Identify the blood parasite species.
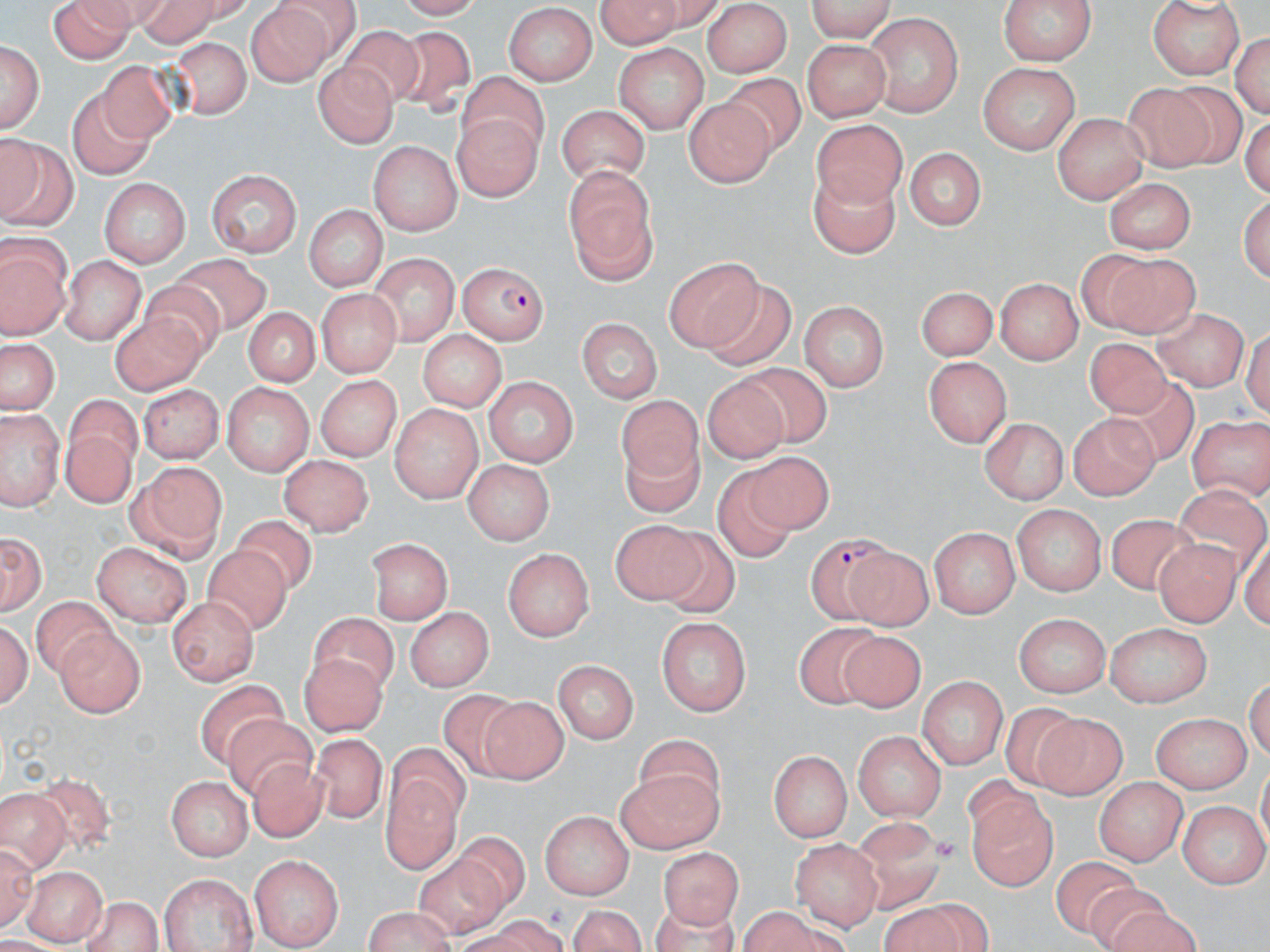

Plasmodium falciparum.

{
  "preparation": "thin blood film",
  "modality": "light microscopy",
  "stain": "May-Grünwald-Giemsa",
  "magnification": "1000x",
  "field_of_view": "one of a larger specimen",
  "image_size": "1270×952 pixels",
  "uninfected_red_blood_cell_locations": "approximate bounding boxes as [x1, y1, x2, y2] in pixels: [47, 0, 133, 63], [126, 0, 220, 46], [592, 0, 722, 41], [800, 0, 896, 40], [1150, 0, 1246, 80], [994, 1, 1101, 64], [250, 2, 343, 83], [505, 5, 595, 84], [705, 7, 789, 74], [865, 14, 967, 117], [339, 21, 424, 113], [396, 26, 477, 119], [1233, 30, 1267, 120], [1, 37, 46, 138], [800, 37, 894, 118], [171, 38, 253, 120], [614, 41, 708, 134], [95, 59, 172, 143], [312, 61, 395, 148], [981, 63, 1078, 153], [457, 70, 545, 166], [724, 73, 813, 158], [1160, 83, 1248, 163], [1123, 87, 1216, 171], [71, 90, 156, 177], [685, 95, 773, 189], [556, 101, 656, 189], [453, 108, 543, 204], [1052, 113, 1150, 199], [811, 120, 908, 206], [0, 133, 69, 233], [368, 138, 462, 236], [907, 143, 987, 230], [562, 162, 663, 286], [810, 165, 901, 268], [207, 169, 302, 258], [1103, 175, 1196, 253], [103, 179, 190, 266], [305, 204, 385, 292], [1, 234, 72, 339], [1085, 248, 1198, 334], [665, 254, 764, 349], [172, 255, 271, 323], [368, 255, 458, 349], [59, 256, 144, 343], [699, 275, 793, 368], [992, 277, 1085, 363], [137, 281, 225, 356], [915, 284, 998, 359], [315, 288, 405, 375], [798, 301, 889, 392], [242, 307, 324, 388], [1154, 309, 1246, 391], [111, 313, 208, 400], [580, 318, 661, 403], [418, 331, 505, 413], [2, 338, 55, 415], [1080, 339, 1175, 421], [923, 354, 1015, 447], [742, 363, 839, 445], [701, 374, 790, 463], [314, 376, 397, 461], [1101, 376, 1199, 469], [483, 377, 580, 470], [139, 384, 221, 462], [222, 385, 312, 474], [331, 386, 459, 474], [615, 390, 708, 481], [60, 398, 142, 510], [391, 403, 482, 502], [2, 410, 60, 508], [1069, 414, 1157, 500], [977, 417, 1071, 502], [1186, 418, 1270, 503], [621, 431, 702, 517], [741, 452, 835, 535], [277, 455, 371, 537], [463, 459, 554, 546], [137, 464, 226, 544], [714, 465, 800, 562], [1176, 484, 1268, 576], [1013, 503, 1103, 598], [231, 511, 324, 585], [1106, 515, 1201, 596], [609, 520, 709, 609], [928, 524, 1021, 616], [655, 526, 743, 615], [1, 529, 46, 616], [366, 535, 454, 621], [1153, 540, 1246, 626], [868, 541, 931, 630], [93, 542, 192, 625], [201, 543, 294, 636], [502, 547, 592, 643], [167, 593, 257, 687], [30, 594, 115, 680], [402, 606, 496, 689], [306, 610, 403, 694], [1015, 612, 1111, 699], [1, 613, 35, 713], [656, 616, 751, 714], [791, 619, 885, 719], [1107, 621, 1213, 707], [53, 626, 145, 716], [836, 631, 927, 715], [298, 656, 392, 735], [551, 657, 639, 742], [918, 674, 1005, 772], [196, 682, 288, 764], [433, 690, 528, 778], [483, 692, 565, 785], [1003, 703, 1090, 791], [220, 711, 319, 801], [1153, 712, 1253, 792], [1034, 716, 1126, 800], [854, 729, 944, 823], [634, 735, 726, 823], [313, 736, 389, 825], [771, 747, 852, 841], [246, 755, 335, 842], [615, 764, 721, 852], [387, 767, 461, 873], [40, 772, 119, 854], [168, 773, 253, 858], [1096, 773, 1188, 865], [0, 787, 72, 878], [967, 798, 1057, 893], [1180, 803, 1268, 886], [540, 810, 633, 900], [847, 817, 946, 915], [456, 828, 533, 911], [793, 842, 881, 929], [658, 846, 741, 930], [409, 853, 508, 936], [251, 854, 341, 949], [1055, 855, 1134, 938], [21, 866, 107, 945], [156, 873, 256, 952], [1080, 881, 1169, 952], [81, 896, 167, 952], [570, 897, 645, 951], [654, 902, 738, 952], [883, 903, 970, 952], [361, 906, 460, 952], [741, 906, 822, 952], [1108, 907, 1211, 952], [487, 918, 565, 952]",
  "platelet_locations": "approximate bounding boxes as [x1, y1, x2, y2] in pixels: [935, 835, 959, 863], [545, 905, 569, 924]",
  "plasmodium_falciparum_infected_red_blood_cell_locations": "approximate bounding boxes as [x1, y1, x2, y2] in pixels: [454, 261, 548, 344], [808, 536, 904, 627]"
}